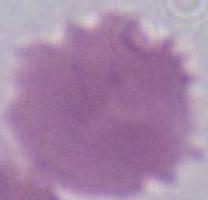
identification = erythrocyte
modality = micrograph
magnification = 1000x